Report the malaria status of this cell.
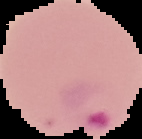

It is parasitized.

Summary:
  - Preparation: thin blood film
  - Image type: segmented cell region with the area outside set to black
  - Image size: 142×139 pixels